Outline each Plasmodium falciparum-infected red blood cell.
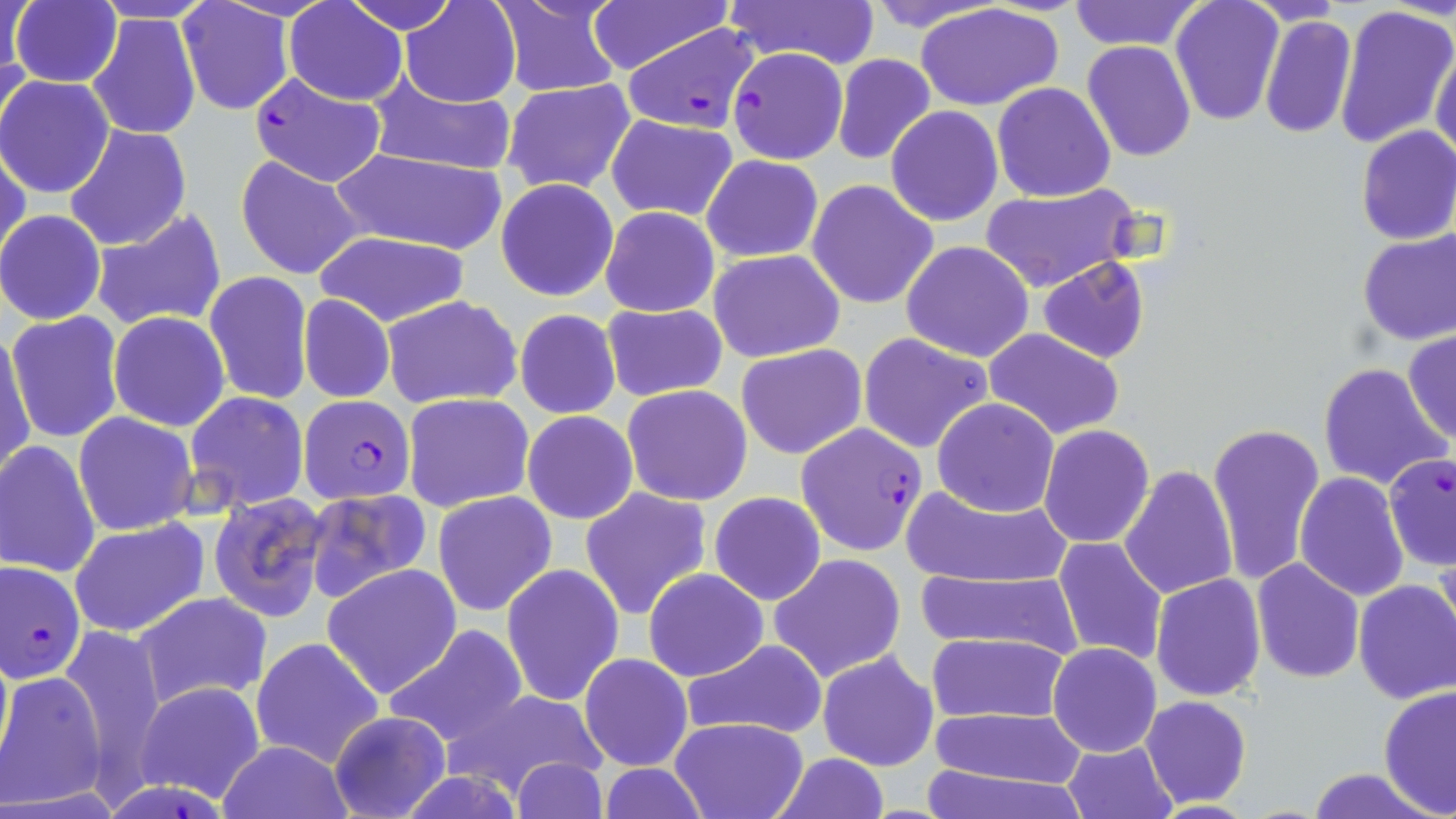
Approximate bounding boxes as (x1, y1, x2, y2) in pixels.
Plasmodium falciparum-infected red blood cells: (621, 24, 759, 134), (728, 47, 849, 164), (249, 73, 387, 188), (299, 396, 414, 504), (795, 422, 927, 557), (1383, 453, 1456, 571), (2, 560, 88, 683), (107, 773, 227, 817).

Summary:
  - Uninfected red blood cell locations: (0, 0, 32, 105), (11, 0, 123, 88), (398, 0, 521, 107), (490, 0, 623, 97), (586, 0, 736, 72), (723, 0, 881, 71), (859, 0, 1009, 34), (1068, 0, 1204, 51), (88, 1, 222, 25), (176, 1, 295, 118), (285, 1, 407, 104), (342, 1, 460, 35), (1171, 1, 1285, 124), (917, 4, 1064, 112), (1332, 5, 1455, 151), (86, 11, 200, 141), (1258, 14, 1356, 140), (1081, 41, 1196, 163), (1431, 43, 1456, 164), (832, 53, 936, 165), (0, 75, 117, 200), (367, 76, 520, 176), (500, 79, 638, 196), (991, 82, 1116, 202), (886, 106, 1002, 227), (606, 114, 739, 223), (63, 125, 192, 252), (1354, 126, 1456, 246), (1, 145, 28, 269), (329, 147, 510, 255), (234, 153, 367, 280), (703, 155, 823, 262), (495, 178, 619, 302), (807, 180, 938, 310), (980, 182, 1141, 296), (600, 205, 720, 317), (89, 209, 227, 334), (0, 210, 106, 325), (1356, 229, 1456, 344), (314, 231, 470, 326), (901, 240, 1035, 362), (709, 249, 845, 362), (1039, 257, 1150, 364), (203, 272, 313, 405), (298, 294, 395, 403), (381, 294, 522, 410), (601, 302, 729, 400), (514, 308, 622, 419), (6, 310, 126, 446), (109, 311, 231, 430), (1, 329, 38, 483), (985, 329, 1127, 440), (1402, 330, 1455, 445), (858, 332, 994, 454), (736, 344, 868, 460), (1318, 361, 1451, 491), (623, 384, 752, 505), (185, 391, 309, 511), (404, 392, 534, 512), (931, 398, 1058, 517), (522, 410, 638, 524), (73, 412, 198, 536), (1207, 421, 1325, 587), (1039, 425, 1154, 548), (0, 440, 101, 580), (1119, 464, 1239, 600), (1295, 472, 1409, 601), (899, 483, 1073, 590), (579, 485, 713, 621), (303, 486, 434, 603), (432, 491, 557, 616), (209, 492, 331, 620), (708, 492, 826, 606), (69, 518, 210, 637), (1053, 537, 1167, 666), (769, 554, 907, 684), (1251, 557, 1364, 683), (321, 564, 462, 700), (500, 564, 624, 706), (643, 568, 768, 682), (917, 570, 1085, 661), (1151, 573, 1266, 701), (1353, 579, 1456, 705), (131, 592, 273, 710), (383, 625, 527, 752), (57, 629, 172, 782), (924, 632, 1073, 726), (250, 636, 385, 770), (678, 639, 829, 741), (1047, 642, 1161, 758), (817, 649, 939, 772), (579, 654, 692, 771), (2, 671, 108, 807), (135, 680, 266, 803), (1378, 685, 1456, 814), (445, 689, 608, 802), (1141, 695, 1252, 808), (925, 708, 1088, 789), (327, 709, 452, 819), (670, 717, 808, 819), (217, 739, 353, 818), (1062, 739, 1177, 819), (770, 753, 888, 818), (510, 756, 610, 819), (918, 761, 1088, 819), (595, 764, 712, 819), (1305, 767, 1440, 819)
  - Slide-level diagnosis: Plasmodium falciparum
  - Preparation: thin blood film
  - Image size: 1456×819 pixels
  - Stain: May-Grünwald-Giemsa
  - Field of view: single
  - Magnification: 1000x
  - Modality: light microscopy